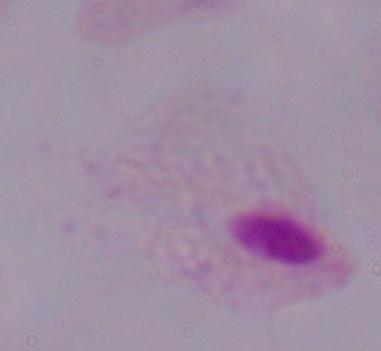

{
  "magnification": "1000x",
  "identification": "trichomonad",
  "modality": "micrograph"
}